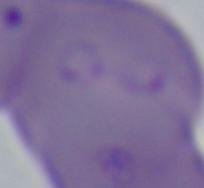

magnification = 1000x
modality = photomicrograph
identification = Babesia